Report the malaria status of this cell.
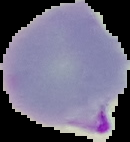

Parasitized.

From a thin blood film. Image is 130×142 pixels. The area outside the segmented cell region is set to black.